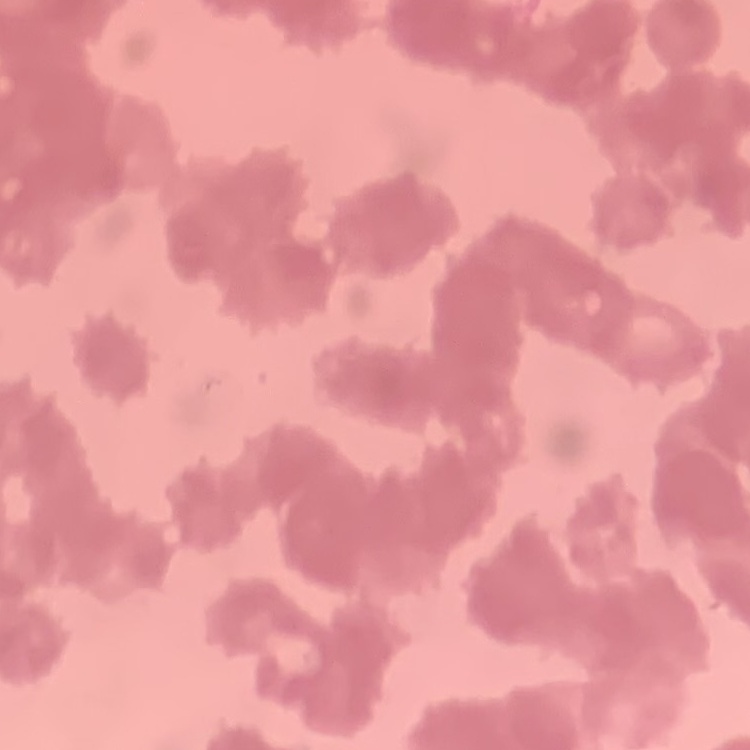
red blood cell morphology = rouleaux formation
preparation = thin blood smear
stain = Field's or Giemsa
image type = one tile cut from a larger photomicrograph